Assess this cell for malaria.
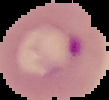
Parasitized.

preparation = thin blood smear
image type = cell region segmented out of the field of view; surrounding area masked to black
image size = 109×100 pixels